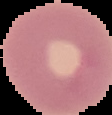

From a thin blood film. Image is 112×115 pixels. Segmented cell region on a black background. Result: negative for malaria parasites.